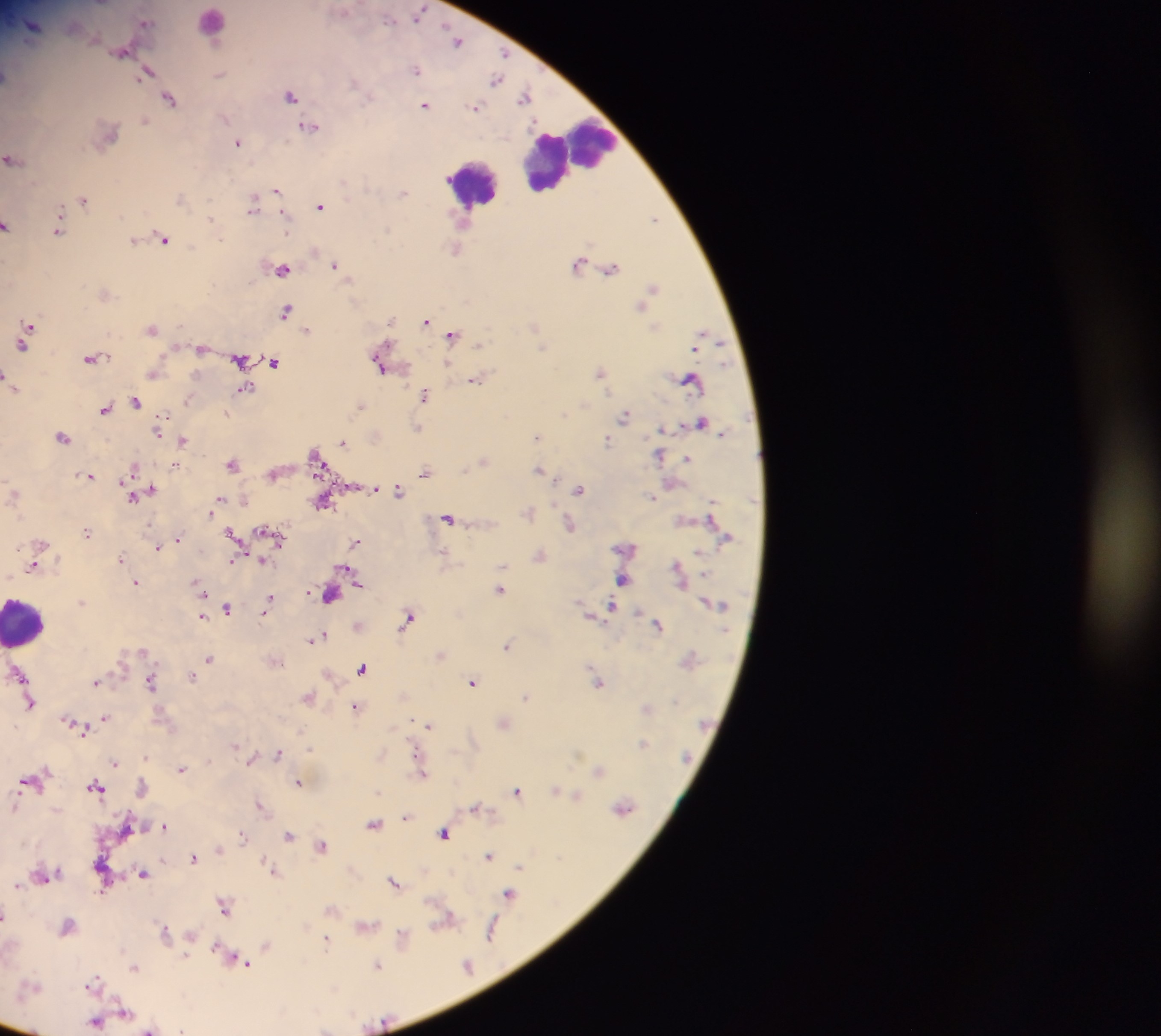 Approximate centers as (x, y) in pixels. Leukocyte locations: (211, 22), (570, 155), (551, 160), (473, 182), (26, 622). Malaria parasite locations: (418, 12), (146, 21), (33, 24), (459, 39), (123, 50), (504, 53), (416, 68), (148, 72), (220, 73), (496, 79), (291, 93), (526, 96), (171, 98), (425, 103), (475, 106), (146, 120), (310, 125), (238, 141), (13, 158), (277, 190), (403, 193), (84, 198), (181, 198), (254, 203), (320, 205), (655, 218), (213, 219), (8, 224), (58, 229), (164, 237), (134, 239), (456, 247), (579, 263), (335, 264), (283, 267), (611, 267), (653, 287), (642, 302), (287, 310), (427, 320), (30, 325), (534, 325), (152, 327), (308, 328), (454, 334), (27, 335), (702, 338), (202, 346), (92, 357), (240, 358), (275, 361), (379, 362), (601, 370), (154, 372), (476, 379), (692, 379), (14, 385), (245, 388), (426, 393), (137, 399), (188, 399), (361, 405), (106, 407), (227, 412), (626, 414), (163, 416), (701, 422), (162, 423), (418, 427), (158, 431), (62, 435), (537, 436), (607, 439), (183, 440), (343, 442), (660, 454), (317, 457), (688, 457), (483, 460), (233, 462), (175, 464), (134, 469), (540, 469), (426, 470), (274, 473), (89, 475), (375, 487), (399, 488), (580, 488), (151, 489), (14, 493), (135, 494), (653, 496), (221, 498), (323, 502), (212, 511), (529, 511), (449, 517), (569, 523), (88, 531), (270, 531), (234, 535), (178, 538), (175, 541), (357, 541), (41, 542), (158, 546), (627, 547), (539, 554), (121, 557), (263, 560), (232, 561), (34, 565), (680, 571), (352, 574), (624, 578), (136, 581), (200, 587), (501, 588), (331, 594), (271, 599), (83, 601), (612, 605), (228, 607), (266, 610), (593, 615), (202, 616), (409, 616), (358, 624), (658, 624), (316, 637), (508, 644), (142, 650), (440, 653), (209, 658), (363, 667), (21, 673), (192, 675), (96, 680), (474, 680), (151, 681), (598, 681), (526, 695), (308, 696), (31, 702), (356, 706), (647, 707), (106, 716), (68, 719), (503, 722), (429, 724), (81, 727), (643, 742), (235, 744), (279, 752), (147, 756), (252, 759), (115, 761), (182, 768), (600, 770), (422, 771), (31, 780), (299, 781), (97, 785), (143, 787), (556, 789), (517, 790), (577, 793), (261, 804), (15, 805), (475, 806), (624, 806), (407, 816), (375, 822), (165, 825), (446, 832), (243, 835), (289, 835), (322, 844), (219, 848), (490, 855), (194, 856), (520, 865), (274, 870), (144, 872), (42, 874), (394, 881), (18, 884), (509, 892), (225, 904), (6, 914), (445, 919), (67, 924), (366, 924), (492, 930), (166, 932), (191, 935), (403, 935), (326, 938), (267, 944), (242, 960), (378, 964), (468, 964), (135, 966), (94, 982), (126, 1011), (97, 1022), (150, 1031). Thick blood smear. Collected in Ghana. Photographed through a microscope with a mobile-phone camera. Image is 1161×1036 pixels. Single field of view.